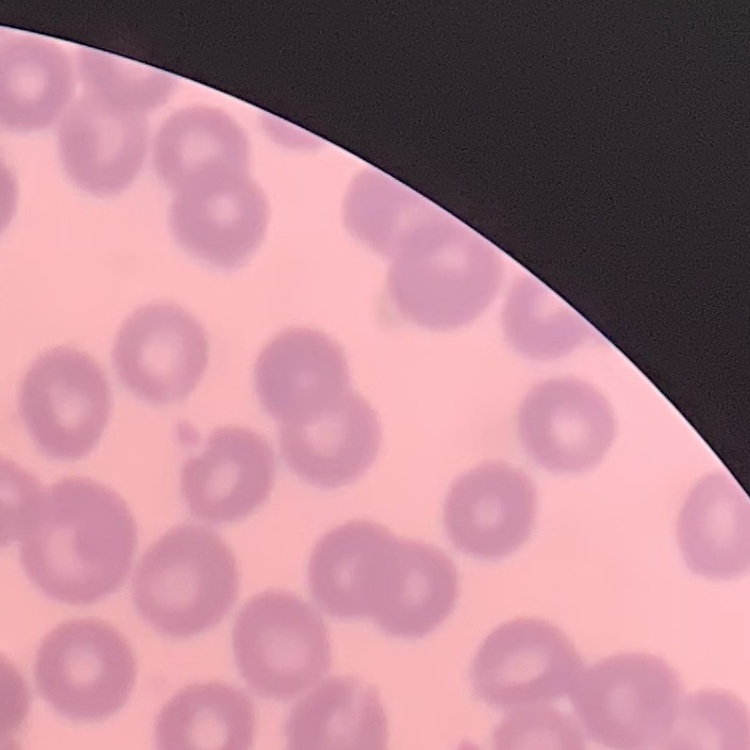

red_blood_cell_morphology: no rouleaux formation
image_type: one tile cut from a larger photomicrograph
stain: Field's or Giemsa
preparation: thin blood smear